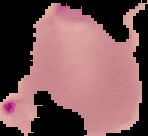
Summary:
  - Image type: segmented cell region on a black background
  - Result: Plasmodium parasites identified
  - Image size: 148×136 pixels
  - Preparation: thin blood film